Classify this cell by malaria status.
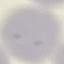

It is uninfected.

Photographed with a smartphone camera at the microscope eyepiece. Giemsa stain. Thin blood film. Automatically extracted cell patch, resized to 64 × 64 pixels.